Outline platelets.
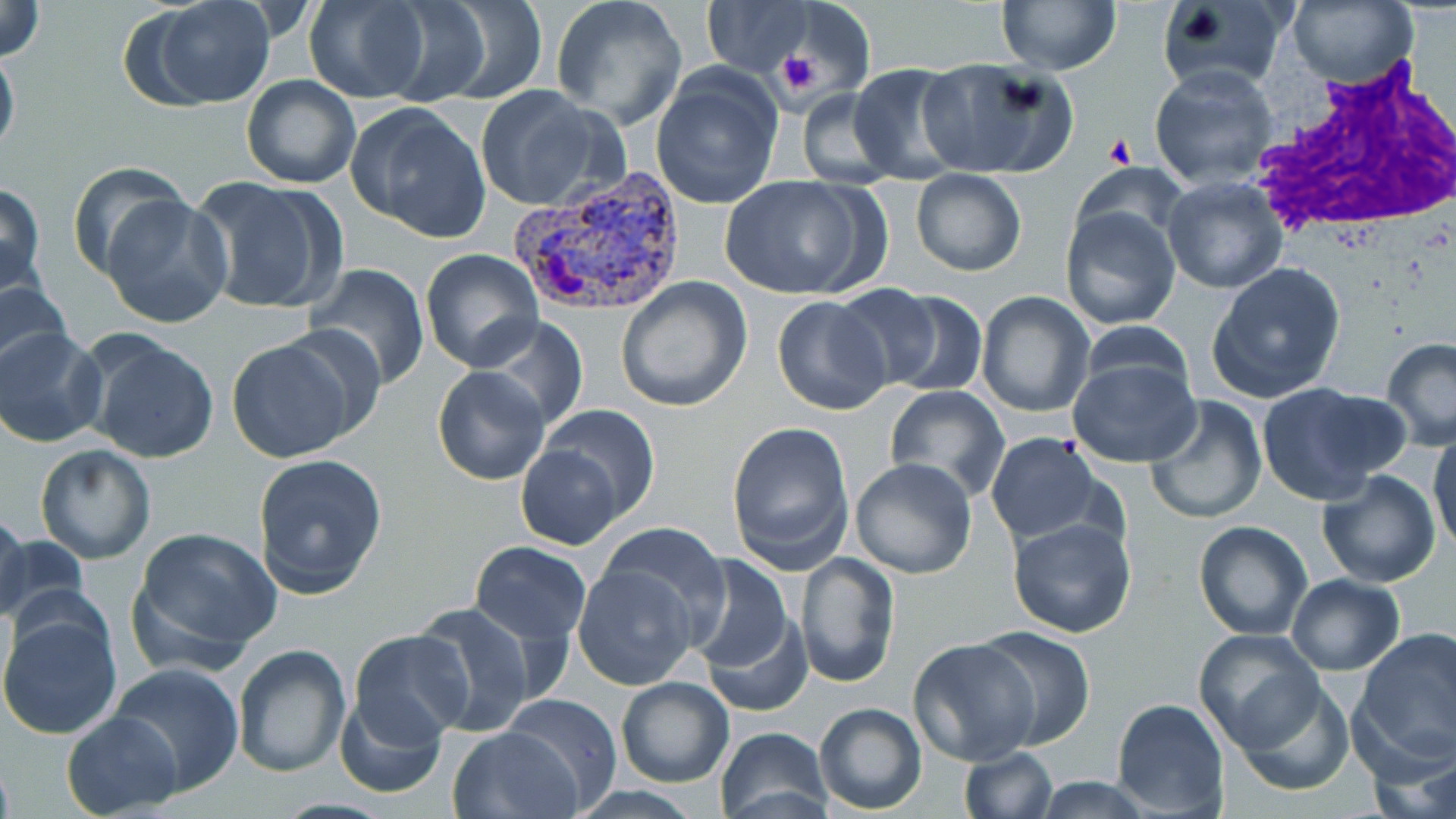

Approximate bounding boxes as (x1,y1)-(x2,y2) corner pairs in pixels.
Platelets: (776,50)-(823,95), (1105,135)-(1134,165).

White blood cell locations: (1245,56)-(1456,241). Plasmodium vivax-infected red blood cell locations: (505,168)-(692,320). Uninfected red blood cell locations: (143,0)-(277,106), (303,0)-(432,104), (550,0)-(690,129), (997,0)-(1122,74), (1287,0)-(1418,89), (0,1)-(48,62), (399,2)-(547,105), (703,2)-(812,77), (1158,3)-(1286,94), (780,5)-(869,99), (0,40)-(20,164), (916,57)-(1077,179), (1149,64)-(1278,189), (848,65)-(970,183), (650,70)-(782,210), (241,75)-(360,188), (473,86)-(614,212), (796,88)-(898,187), (348,103)-(491,241), (66,159)-(191,281), (1072,164)-(1189,255), (910,170)-(1027,277), (719,175)-(875,301), (188,176)-(347,315), (1160,177)-(1289,295), (0,182)-(47,296), (103,195)-(233,329), (1059,204)-(1183,331), (420,249)-(544,372), (1205,261)-(1346,404), (309,264)-(431,391), (0,275)-(72,375), (615,278)-(753,413), (861,287)-(988,396), (975,292)-(1095,418), (771,295)-(892,416), (477,316)-(589,432), (1079,320)-(1196,401), (1,326)-(106,447), (82,334)-(220,462), (224,336)-(359,463), (1381,339)-(1456,451), (1069,355)-(1201,469), (432,365)-(550,486), (1254,382)-(1403,506), (884,386)-(1010,500), (1145,396)-(1268,525), (540,403)-(660,520), (725,421)-(854,571), (1429,431)-(1456,556), (985,432)-(1103,543), (35,445)-(156,564), (516,445)-(624,548), (252,454)-(387,600), (849,457)-(978,579), (1317,469)-(1440,587), (0,509)-(30,625), (1009,517)-(1138,639), (593,521)-(732,632), (1193,521)-(1312,640), (131,526)-(282,664), (0,528)-(90,634), (469,540)-(591,646), (583,542)-(784,678), (684,552)-(800,690), (793,552)-(899,689), (573,564)-(699,689), (1284,573)-(1405,675), (700,600)-(814,721), (409,602)-(539,737), (0,610)-(124,741), (976,627)-(1095,750), (1193,628)-(1326,753), (1353,628)-(1456,770), (349,630)-(474,744), (909,637)-(1039,766), (231,642)-(349,776), (109,663)-(244,794), (615,676)-(737,788), (1235,679)-(1356,796), (333,691)-(445,800), (497,692)-(625,809), (1112,698)-(1229,817), (813,702)-(926,814), (62,710)-(182,817), (449,726)-(585,819), (712,726)-(833,818), (1372,739)-(1456,819), (958,747)-(1058,818), (1028,777)-(1159,817). Slide-level diagnosis: Plasmodium vivax. Thin blood smear. One field of a larger specimen. Light microscopy. Image is 1456×819 pixels. May-Grünwald-Giemsa stain. 1000x magnification.